Classify this cell by malaria status.
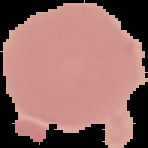
Uninfected.

image type = cell region segmented out of the field of view; surrounding area masked to black
image size = 148×148 pixels
preparation = thin blood film